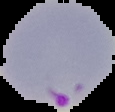
From a thin blood smear. Result: Plasmodium parasites identified. Segmented cell region on a black background. Image is 115×112 pixels.